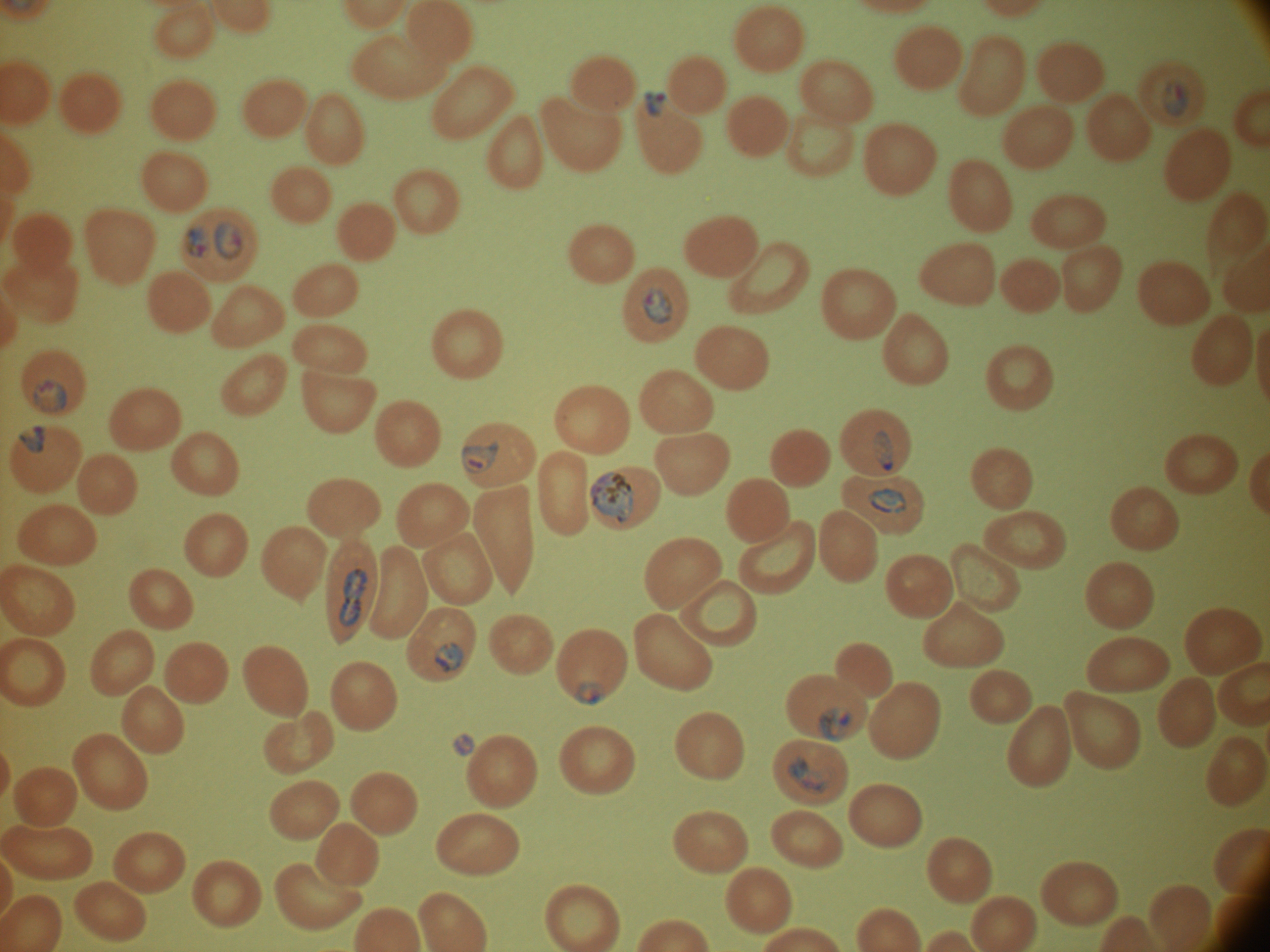 Approximate bounding boxes as named x1/y1/x2/y2 corners in pixels, from the source annotation, which is not necessarily exhaustive. Ring form locations: (x1=212, y1=217, x2=247, y2=263), (x1=183, y1=225, x2=208, y2=262), (x1=30, y1=377, x2=70, y2=414), (x1=16, y1=421, x2=47, y2=456), (x1=458, y1=440, x2=502, y2=475), (x1=575, y1=681, x2=605, y2=707). Schizont locations: (x1=590, y1=468, x2=637, y2=524). Trophozoite locations: (x1=641, y1=287, x2=673, y2=325), (x1=869, y1=429, x2=896, y2=473), (x1=865, y1=486, x2=908, y2=517), (x1=336, y1=566, x2=369, y2=627), (x1=434, y1=640, x2=465, y2=674), (x1=817, y1=706, x2=853, y2=743), (x1=787, y1=755, x2=837, y2=795). Life-cycle stages among the annotated parasites: ring form, trophozoite, schizont. Leica DM2000 optical microscope with a built-in camera. Thin blood film. Giemsa-stained preparation. 100x magnification. Species: Plasmodium falciparum. Single field of view. Image is 1270×952 pixels.